Comment on the morphology of the red blood cells.
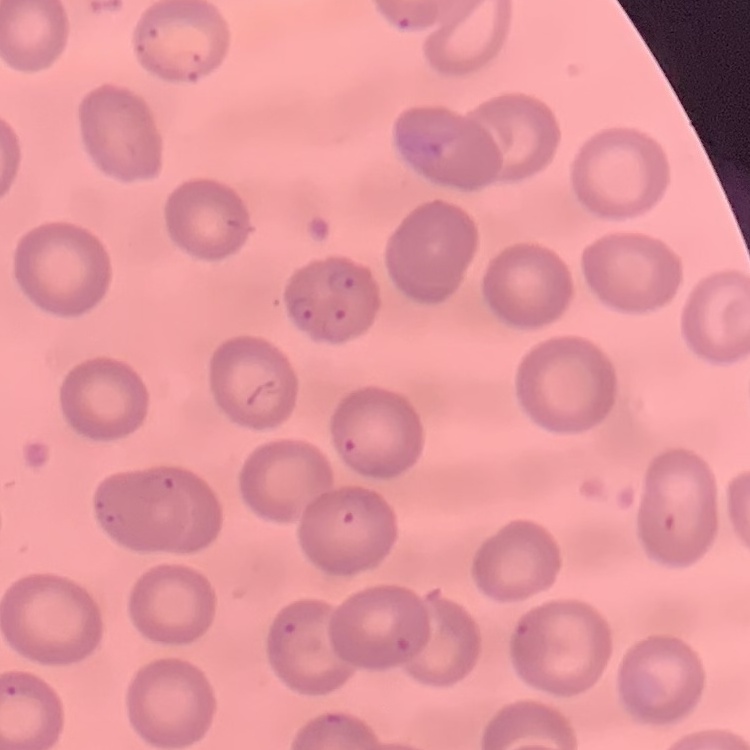
No rouleaux formation.

Summary:
  - Image type: square crop of a larger photomicrograph
  - Stain: Field's or Giemsa
  - Preparation: thin blood smear